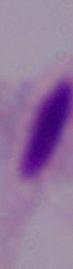

modality = micrograph
identification = trichomonad
magnification = 1000x